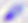
Summary:
  - Modality: photomicrograph
  - Identification: Toxoplasma gondii
  - Magnification: 400x